Classify this cell by malaria status.
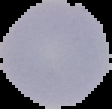

It is uninfected.

image type = segmented cell region with the area outside set to black
image size = 112×109 pixels
preparation = thin blood smear